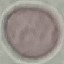

Malaria status: uninfected. Acquired by smartphone through the microscope eyepiece. Giemsa stain. Automatically extracted cell patch, resized to 64 × 64 pixels. Thin blood film.